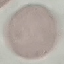
Summary:
  - Malaria status: uninfected
  - Image type: automatically extracted cell patch, resized to 64 × 64 pixels
  - Capture: smartphone camera at the microscope eyepiece
  - Stain: Giemsa
  - Preparation: thin smear